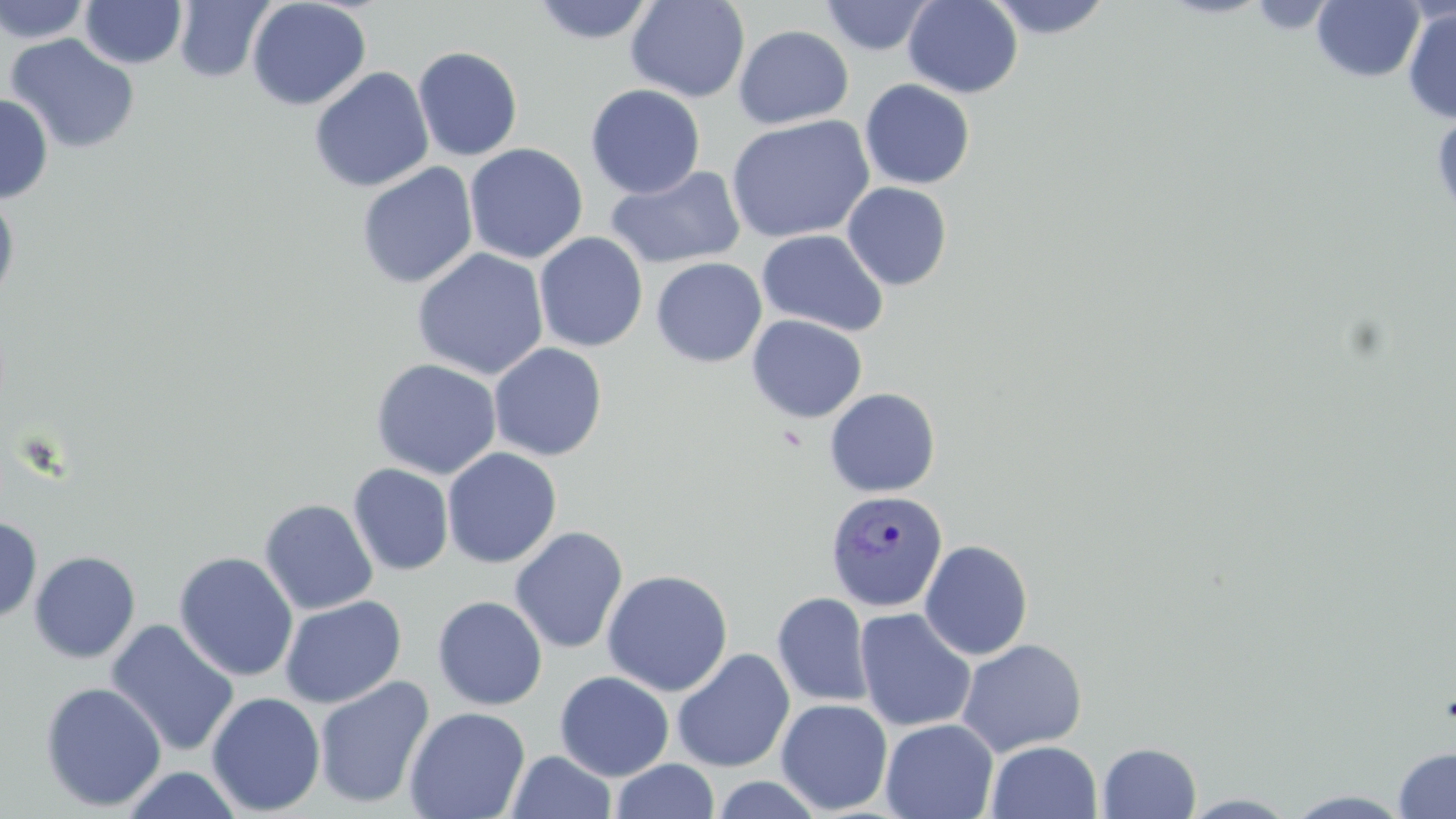

{
  "slide_level_diagnosis": "Plasmodium vivax",
  "stain": "May-Grünwald-Giemsa",
  "image_size": "1456×819 pixels",
  "uninfected_red_blood_cell_locations": "approximate bounding boxes as [x1, y1, x2, y2] in pixels: [0, 0, 93, 44], [173, 0, 275, 84], [247, 0, 371, 111], [530, 0, 658, 45], [626, 0, 750, 103], [821, 0, 937, 56], [903, 0, 1023, 98], [984, 0, 1115, 40], [1311, 0, 1424, 83], [80, 1, 186, 69], [1245, 1, 1338, 34], [1402, 5, 1456, 124], [733, 25, 854, 128], [4, 34, 140, 154], [412, 46, 523, 161], [309, 66, 435, 193], [859, 79, 975, 190], [585, 83, 706, 199], [0, 94, 53, 203], [1430, 110, 1456, 225], [725, 115, 875, 243], [464, 143, 588, 264], [356, 162, 478, 289], [606, 164, 745, 269], [842, 181, 952, 291], [0, 191, 20, 310], [757, 229, 889, 337], [534, 232, 648, 352], [412, 248, 549, 380], [651, 257, 766, 367], [747, 315, 867, 423], [488, 342, 608, 461], [370, 358, 502, 480], [824, 387, 941, 497], [442, 447, 562, 569], [348, 463, 454, 575], [259, 498, 378, 615], [0, 516, 42, 623], [509, 525, 629, 655], [919, 539, 1033, 660], [29, 551, 141, 664], [174, 551, 298, 682], [601, 568, 733, 697], [772, 592, 873, 708], [279, 595, 407, 708], [432, 596, 547, 710], [854, 608, 977, 732], [105, 618, 240, 757], [956, 638, 1087, 756], [672, 649, 795, 773], [555, 671, 674, 780], [313, 675, 435, 809], [39, 681, 167, 812], [206, 691, 326, 816], [776, 698, 893, 815], [404, 706, 531, 819], [880, 717, 998, 819], [986, 740, 1102, 819], [1097, 742, 1201, 819], [1392, 746, 1456, 818], [507, 750, 617, 819], [611, 759, 720, 819], [118, 766, 246, 818], [709, 775, 825, 818], [1284, 790, 1415, 818], [1178, 792, 1301, 818]",
  "plasmodium_vivax_infected_red_blood_cell_locations": "approximate bounding boxes as [x1, y1, x2, y2] in pixels: [825, 489, 948, 612]",
  "preparation": "thin blood smear",
  "field_of_view": "single",
  "magnification": "1000x",
  "modality": "optical microscopy"
}